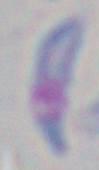

Micrograph. Captured at 1000x magnification. Toxoplasma gondii is shown.